Report the malaria status of this cell.
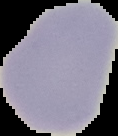

Uninfected.

Summary:
  - Image type: segmented cell region on a black background
  - Preparation: thin blood film
  - Image size: 118×136 pixels